Identify the parasite.
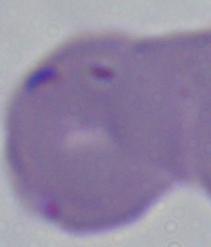

This is Babesia.

Summary:
  - Magnification: 1000x
  - Modality: micrograph